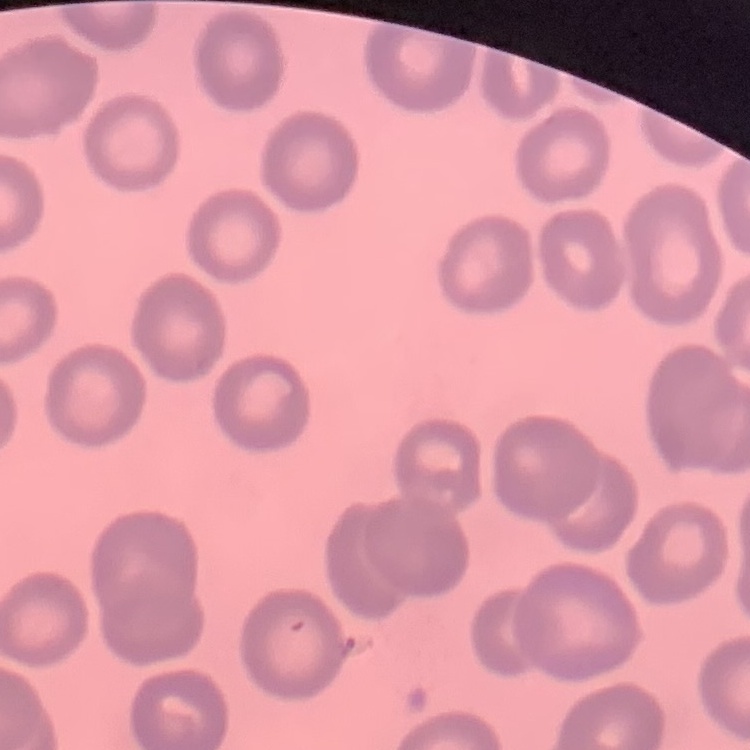

Summary:
  - Erythrocyte morphology: no rouleaux formation
  - Image type: square crop of a larger photomicrograph
  - Preparation: thin blood smear
  - Stain: Field's or Giemsa